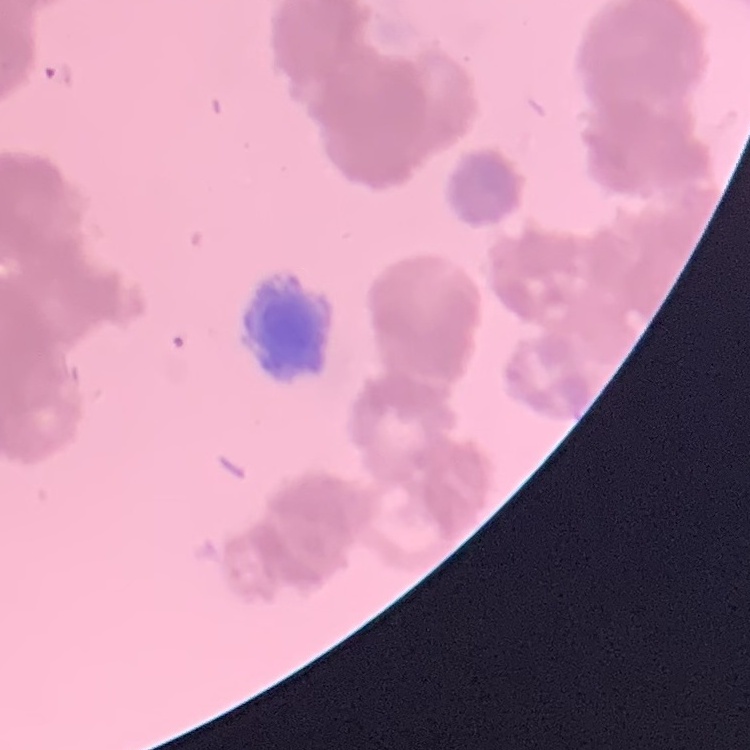
Summary:
  - Erythrocyte morphology: rouleaux formation
  - Stain: Field's or Giemsa
  - Image type: one tile cut from a larger photomicrograph
  - Preparation: thin blood film